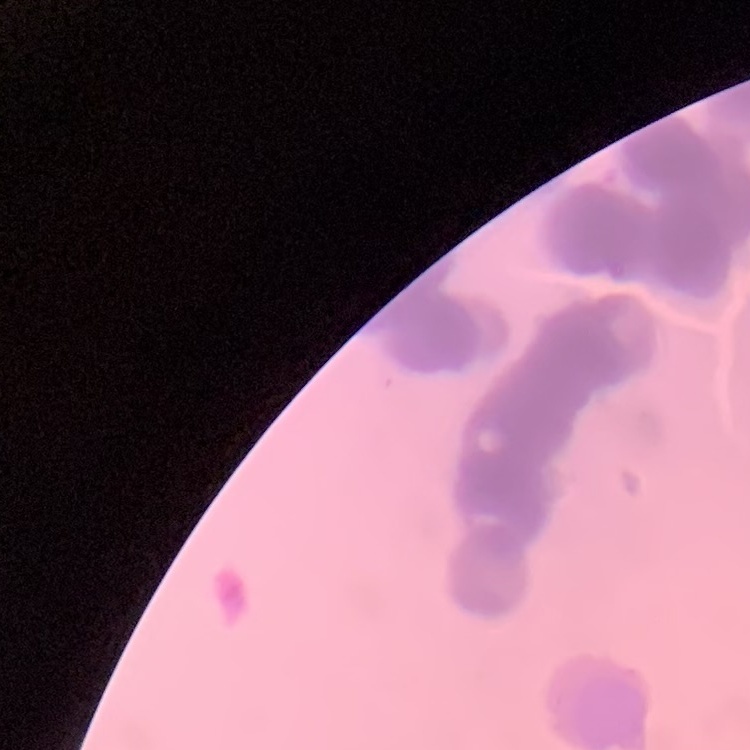 The erythrocytes show rouleaux formation. Square crop of a larger photomicrograph. Stained with either Field's or Giemsa. Thin peripheral smear.